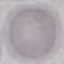
Malaria status: uninfected. Thin blood smear. Acquired by smartphone through the microscope eyepiece. Automatically extracted cell patch, resized to 64 × 64 pixels. Giemsa stain.